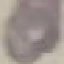
Summary:
  - Malaria status: uninfected
  - Preparation: thin blood smear
  - Capture: smartphone through the microscope eyepiece
  - Stain: Giemsa
  - Image type: automatically extracted cell patch, resized to 64 × 64 pixels